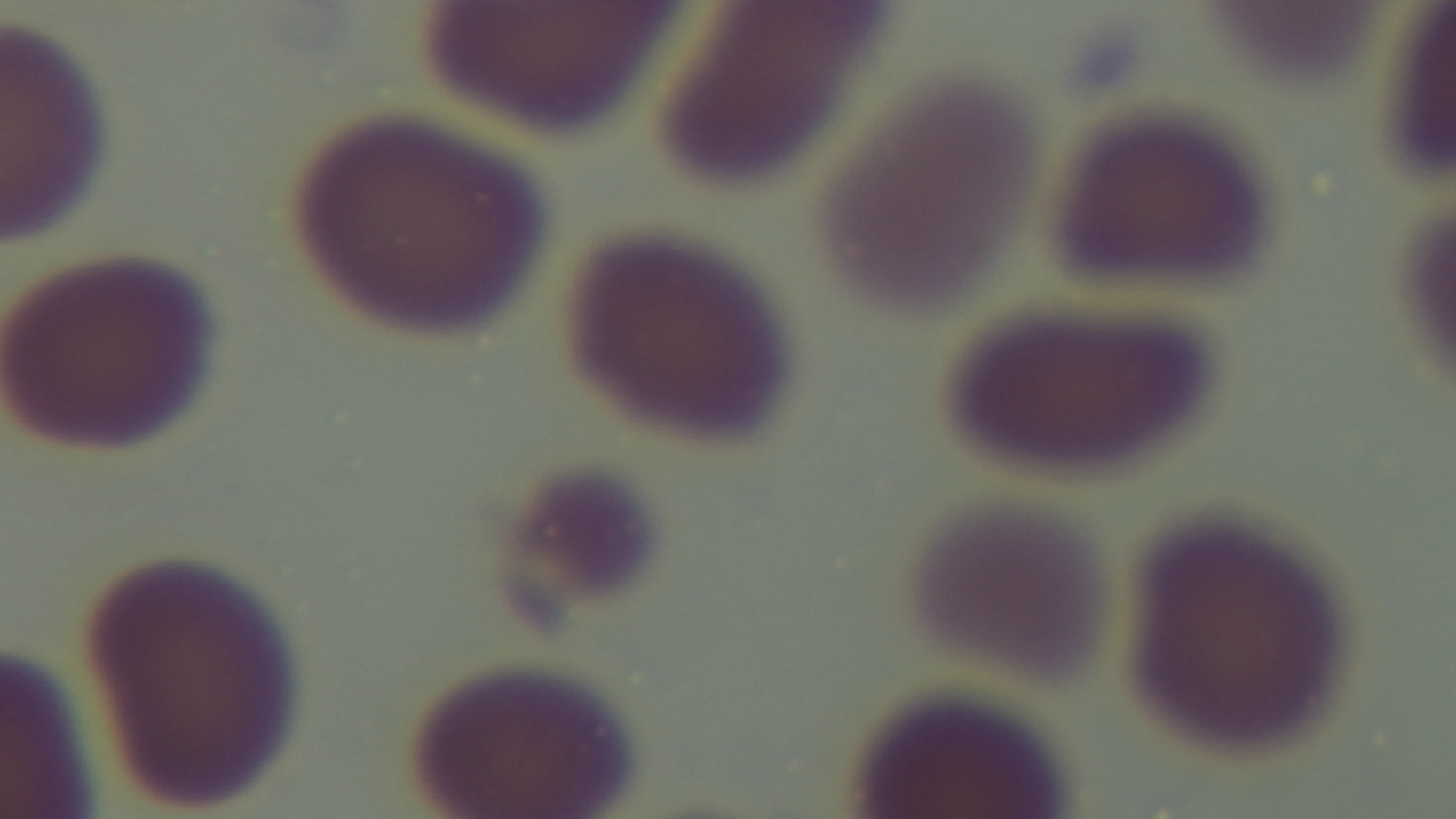

{
  "stain": "Giemsa",
  "preparation": "thin blood film",
  "objective": "100x oil immersion",
  "modality": "light microscopy",
  "field_of_view": "one from the slide",
  "capture": "mounted 4K digital camera",
  "malaria_status": "negative"
}